Look for Plasmodium parasites.
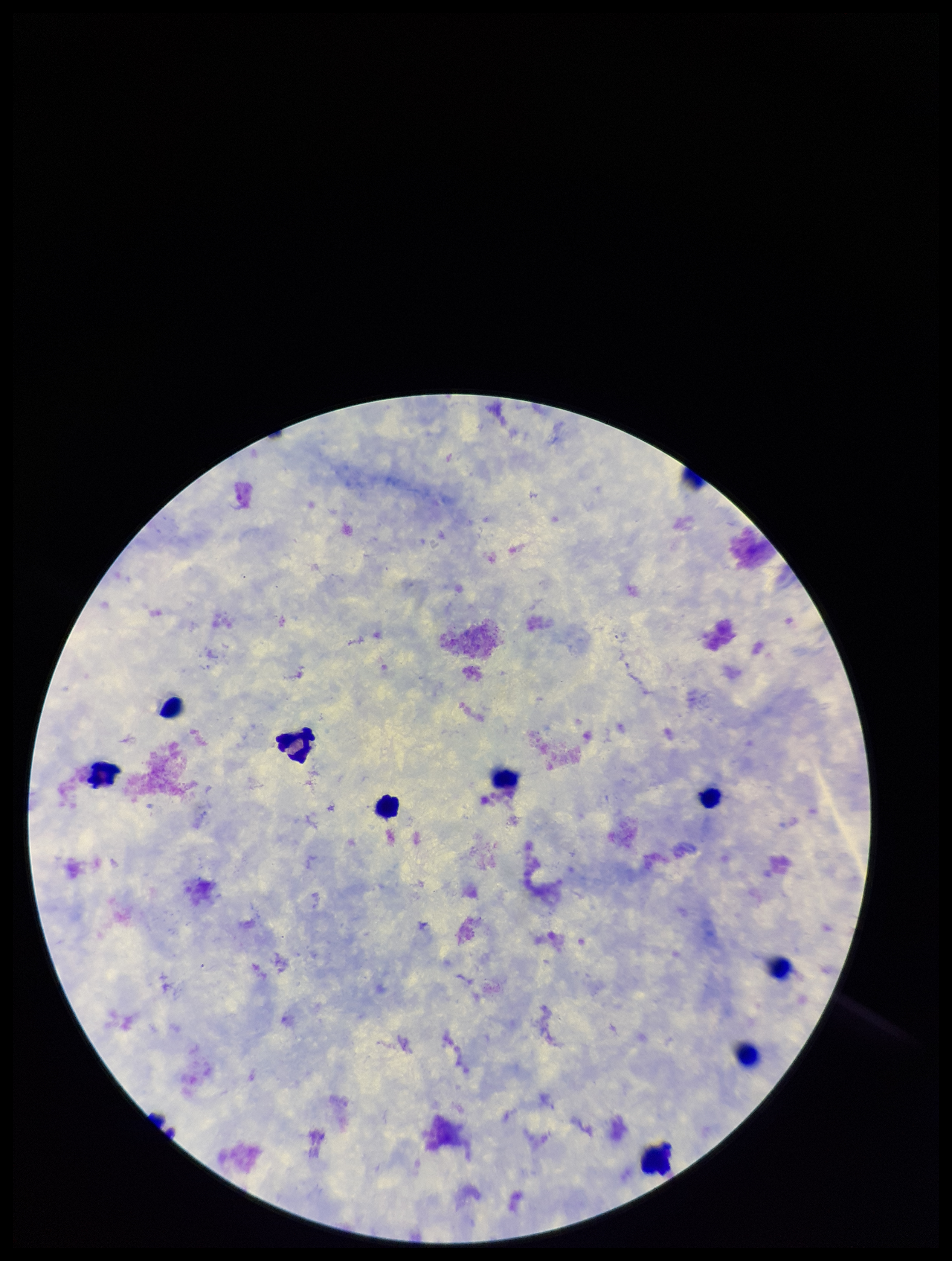
None identified.

Leukocyte count: 9. One field from this slide. Photographed through the microscope eyepiece with a smartphone camera. Patient malaria status: negative. Giemsa stain. Preparation: thick blood smear. Image is 952×1261 pixels. Parasite count: 0.